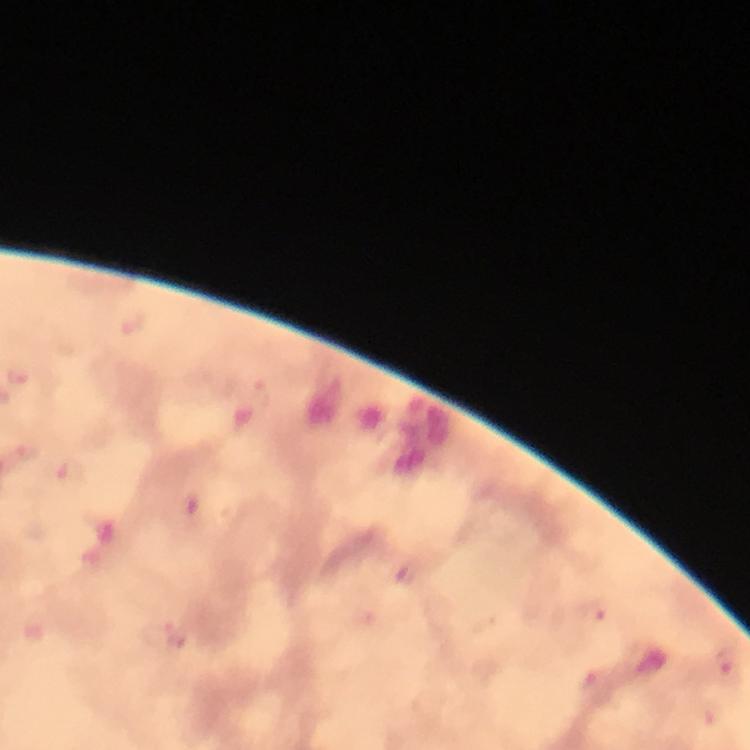
Approximate object centers, in pixels from the top-left corner. Malaria parasite locations: (x=264, y=393), (x=70, y=474), (x=407, y=574), (x=595, y=613), (x=728, y=668). Thick smear. Image is 750×750 pixels. Giemsa stain. A crop from one field of view. At 100x magnification. Photographed through the microscope with a smartphone camera. Immersion oil was used. From a diagnostic examination for malaria.